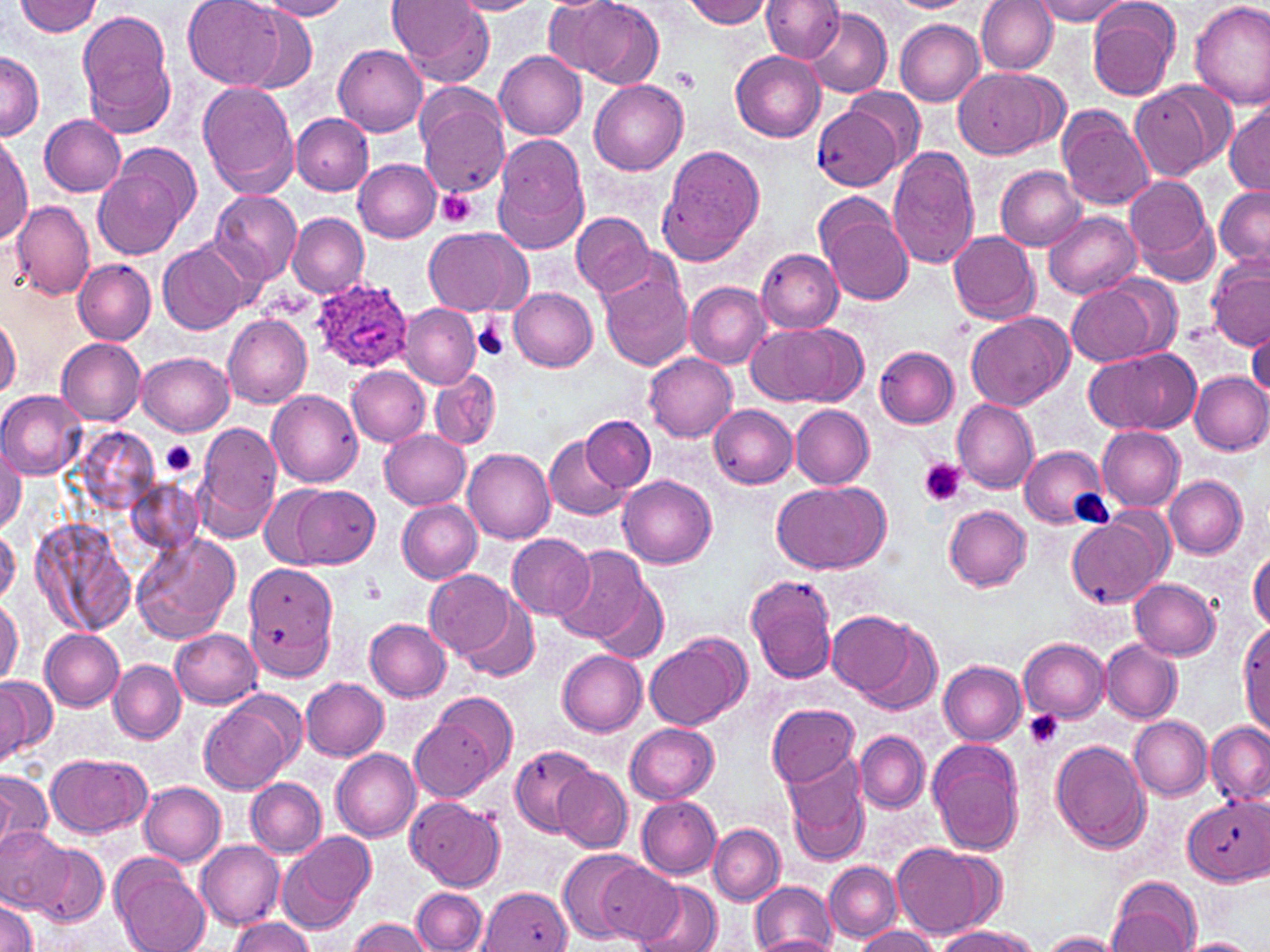

Approximate bounding boxes as [x1, y1, x2, y2] in pixels. Platelet locations: [673, 69, 700, 92], [436, 187, 478, 228], [473, 315, 512, 360], [160, 440, 199, 478], [918, 457, 965, 505], [364, 579, 385, 603], [1023, 711, 1064, 749]. Uninfected red blood cell locations: [15, 0, 103, 37], [186, 0, 288, 88], [388, 0, 496, 85], [449, 0, 543, 16], [551, 0, 666, 88], [761, 0, 845, 63], [977, 0, 1059, 74], [1031, 0, 1133, 23], [1189, 0, 1270, 111], [254, 1, 353, 21], [680, 1, 774, 28], [881, 1, 977, 12], [1086, 1, 1182, 101], [802, 8, 891, 98], [78, 10, 177, 134], [237, 12, 318, 95], [895, 19, 985, 106], [332, 44, 428, 136], [493, 51, 588, 140], [730, 51, 826, 141], [0, 52, 43, 140], [952, 66, 1059, 159], [589, 80, 689, 175], [1130, 80, 1230, 183], [199, 82, 299, 197], [843, 87, 925, 168], [416, 92, 509, 197], [813, 104, 902, 191], [1225, 104, 1270, 195], [1058, 106, 1154, 210], [291, 114, 372, 195], [39, 115, 127, 196], [1, 134, 31, 249], [490, 137, 591, 251], [659, 146, 766, 264], [886, 147, 980, 271], [93, 150, 198, 259], [353, 159, 441, 242], [997, 166, 1086, 250], [1123, 175, 1218, 285], [1215, 186, 1270, 267], [210, 190, 302, 285], [814, 192, 917, 307], [12, 200, 95, 300], [1042, 210, 1141, 298], [287, 212, 369, 298], [571, 212, 654, 298], [424, 227, 531, 316], [948, 230, 1040, 324], [158, 242, 248, 335], [756, 249, 844, 333], [1206, 257, 1270, 352], [74, 259, 157, 344], [598, 264, 692, 372], [1065, 278, 1168, 365], [684, 281, 771, 368], [507, 287, 598, 371], [400, 302, 481, 388], [965, 312, 1073, 410], [221, 313, 312, 408], [0, 316, 21, 399], [748, 324, 841, 406], [791, 325, 869, 405], [1246, 327, 1269, 403], [56, 338, 146, 425], [1084, 346, 1202, 436], [875, 347, 959, 428], [138, 350, 234, 435], [644, 353, 737, 442], [345, 365, 430, 447], [429, 369, 501, 451], [1188, 371, 1270, 454], [0, 390, 85, 478], [266, 390, 363, 487], [952, 398, 1039, 494], [215, 404, 306, 509], [708, 405, 798, 489], [790, 405, 874, 488], [582, 416, 654, 491], [196, 422, 283, 538], [1095, 427, 1184, 511], [380, 430, 471, 509], [544, 433, 629, 521], [0, 441, 24, 534], [1019, 445, 1109, 529], [463, 449, 555, 545], [618, 475, 717, 568], [1164, 475, 1247, 558], [131, 480, 201, 553], [772, 482, 888, 574], [262, 486, 330, 567], [292, 486, 380, 569], [396, 499, 482, 583], [943, 506, 1033, 591], [1065, 512, 1170, 610], [32, 519, 135, 636], [0, 524, 19, 607], [132, 533, 240, 643], [508, 534, 596, 620], [552, 546, 650, 646], [1248, 549, 1270, 634], [244, 564, 340, 681], [424, 568, 523, 660], [745, 574, 838, 683], [1130, 578, 1221, 660], [591, 582, 668, 665], [454, 592, 541, 682], [0, 596, 23, 687], [828, 612, 919, 699], [365, 619, 451, 701], [855, 621, 943, 715], [1238, 621, 1269, 735], [171, 628, 261, 708], [41, 629, 124, 710], [645, 637, 745, 731], [1018, 638, 1109, 722], [1101, 639, 1180, 723], [557, 650, 646, 735], [109, 660, 185, 743], [939, 661, 1027, 745], [0, 674, 54, 764], [301, 678, 387, 760], [199, 696, 297, 797], [766, 704, 860, 787], [410, 712, 503, 803], [1129, 715, 1212, 800], [625, 723, 719, 804], [1204, 723, 1270, 806], [855, 731, 929, 813], [1051, 739, 1151, 854], [929, 741, 1025, 856], [509, 744, 599, 835], [332, 748, 420, 842], [45, 753, 153, 839], [783, 753, 871, 863], [553, 767, 633, 852], [0, 770, 54, 853], [247, 776, 326, 859], [138, 781, 226, 866], [1183, 794, 1269, 884], [406, 796, 504, 893], [636, 796, 721, 880], [708, 824, 783, 905], [0, 826, 69, 912], [277, 829, 375, 933], [197, 841, 284, 928], [890, 841, 998, 938], [27, 842, 110, 924], [558, 848, 645, 943], [111, 857, 211, 952], [596, 859, 683, 943], [825, 860, 901, 941], [1106, 876, 1202, 952], [632, 877, 721, 952], [751, 881, 836, 952], [482, 884, 573, 951], [411, 889, 487, 952], [1, 898, 39, 952], [230, 917, 315, 952], [348, 917, 436, 952], [934, 925, 1040, 951], [854, 926, 940, 952], [1039, 931, 1125, 951], [754, 934, 839, 952], [1175, 938, 1261, 952]. Plasmodium ovale-infected red blood cell locations: [311, 278, 411, 373]. Slide-level diagnosis: Plasmodium ovale. Image is 1270×952 pixels. Thin blood smear. Captured at 1000x magnification. May-Grünwald-Giemsa stain. Optical microscopy. Single field of view.